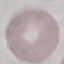
result = no malaria parasites seen
capture = smartphone through the microscope eyepiece
stain = Giemsa
image type = cell patch, automatically extracted from a larger field of view and resized to 64 × 64 pixels
preparation = thin blood film